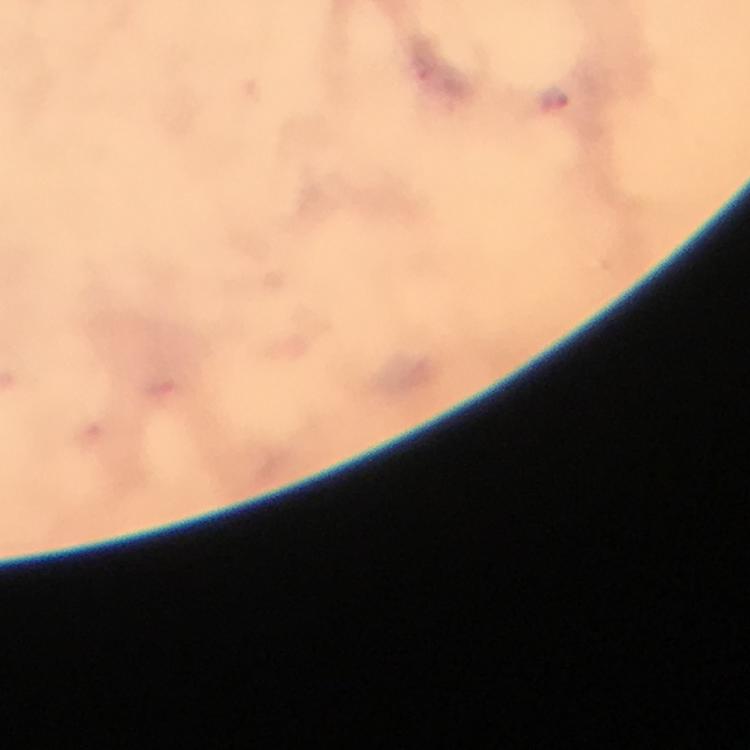

Approximate centers as [x, y] in pixels. Malaria parasite locations: [554, 100]. Smartphone photograph taken through a microscope. From a diagnostic examination for malaria. Immersion oil was used. 100x magnification. Cropped region of a single field of view. Giemsa-stained preparation. Thick blood smear. Image is 750×750 pixels.